Report the malaria status of this cell.
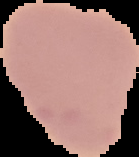
Uninfected.

Image is 139×157 pixels. Cell region segmented out of the field of view; the surrounding area is masked to black. From a thin blood smear.